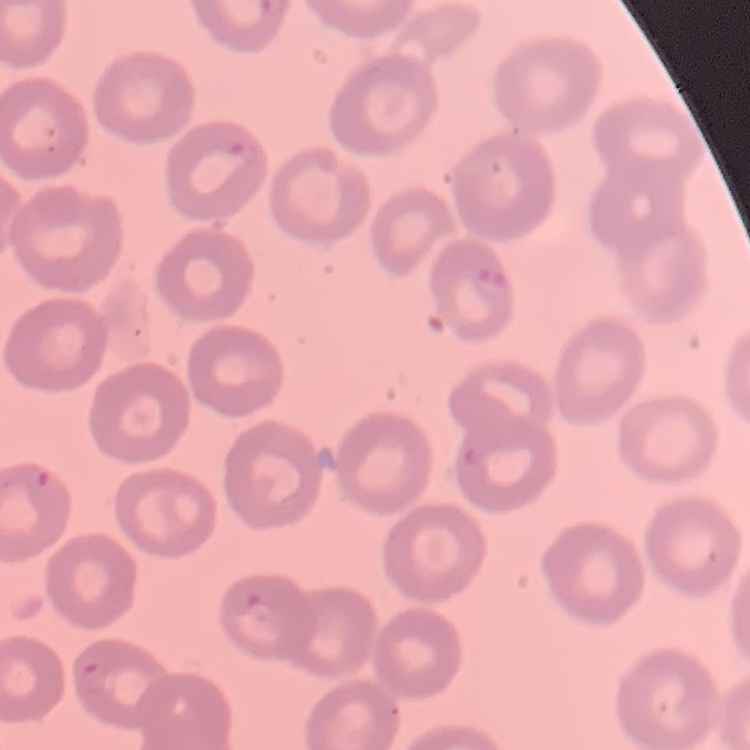

Summary:
  - Red blood cell morphology: no rouleaux formation
  - Image type: square crop of a larger photomicrograph
  - Preparation: thin blood film
  - Stain: Field's or Giemsa